Classify this cell by malaria status.
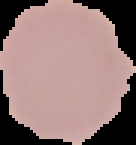
Uninfected.

From a thin blood smear. The area outside the segmented cell region is set to black. Image is 136×145 pixels.